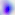
Summary:
  - Magnification: 400x
  - Identification: Toxoplasma gondii
  - Modality: micrograph